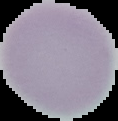

Cell region segmented out of the field of view; the surrounding area is masked to black. Malaria status: uninfected. Image is 118×121 pixels. From a thin blood film.